Describe the morphology of the red blood cells.
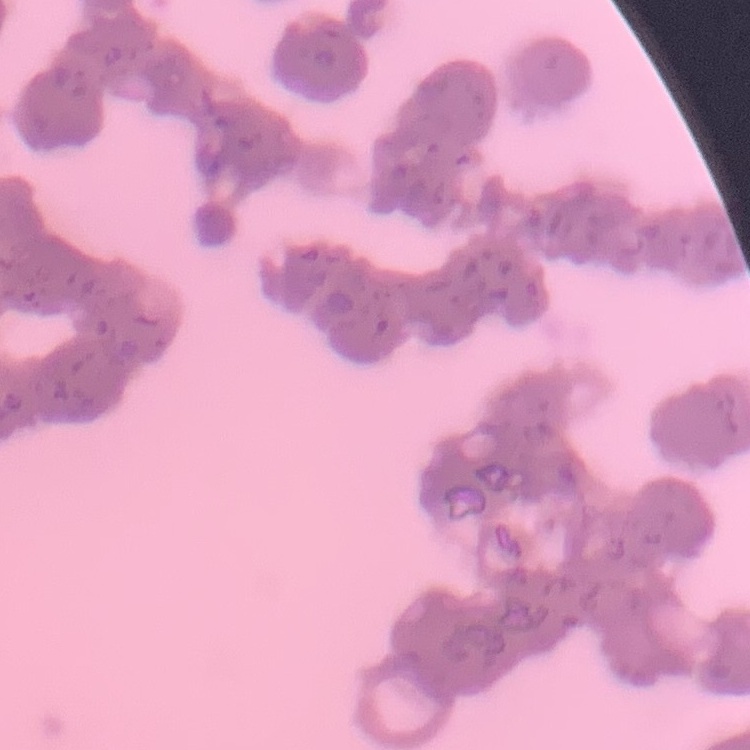

They show rouleaux formation.

image type = square crop of a larger photomicrograph
stain = Field's or Giemsa
preparation = thin blood film